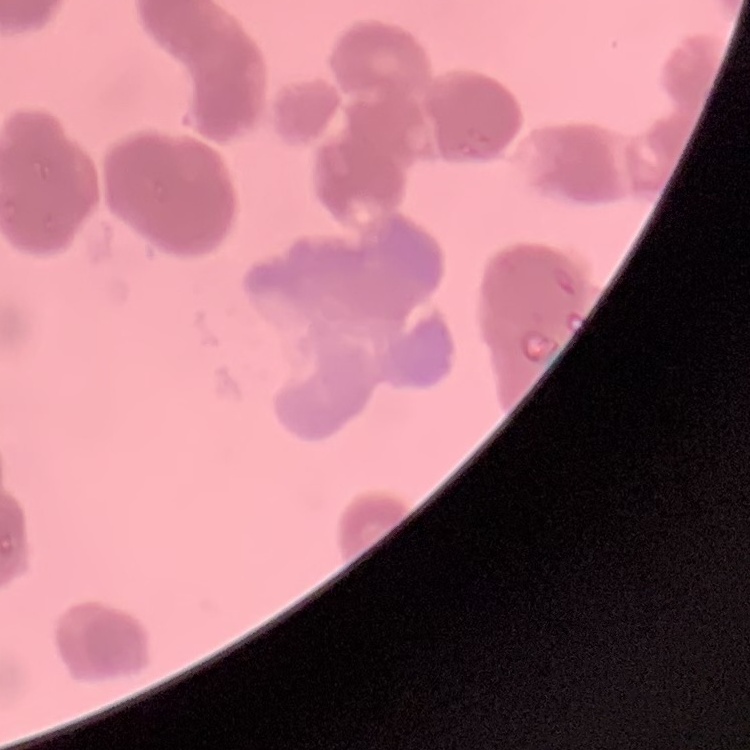

Summary:
  - Erythrocyte morphology: rouleaux formation
  - Preparation: thin blood film
  - Stain: Field's or Giemsa
  - Image type: one tile cut from a larger photomicrograph